Assess this cell for malaria.
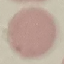
It is uninfected.

{
  "stain": "Giemsa",
  "image_type": "automatically extracted cell patch, resized to 64 × 64 pixels",
  "capture": "smartphone through the microscope eyepiece",
  "preparation": "thin smear"
}